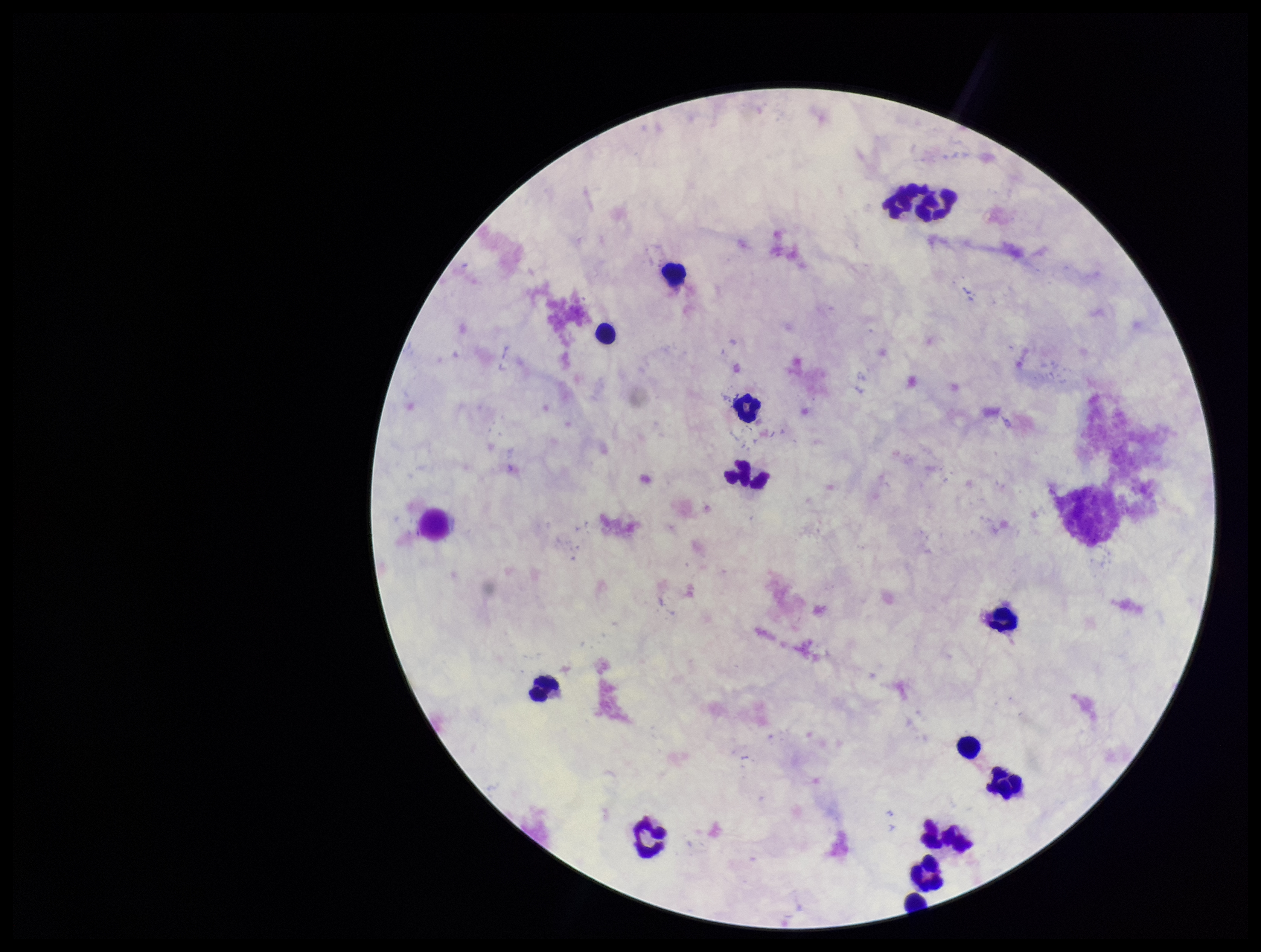
parasite count = 0
Plasmodium parasites = none detected
field of view = one from this slide
preparation = thick blood smear
image size = 1261×952 pixels
leukocyte count = 14
capture = smartphone photograph through the microscope eyepiece
stain = Giemsa
patient malaria status = negative